Describe the morphology of the red blood cells.
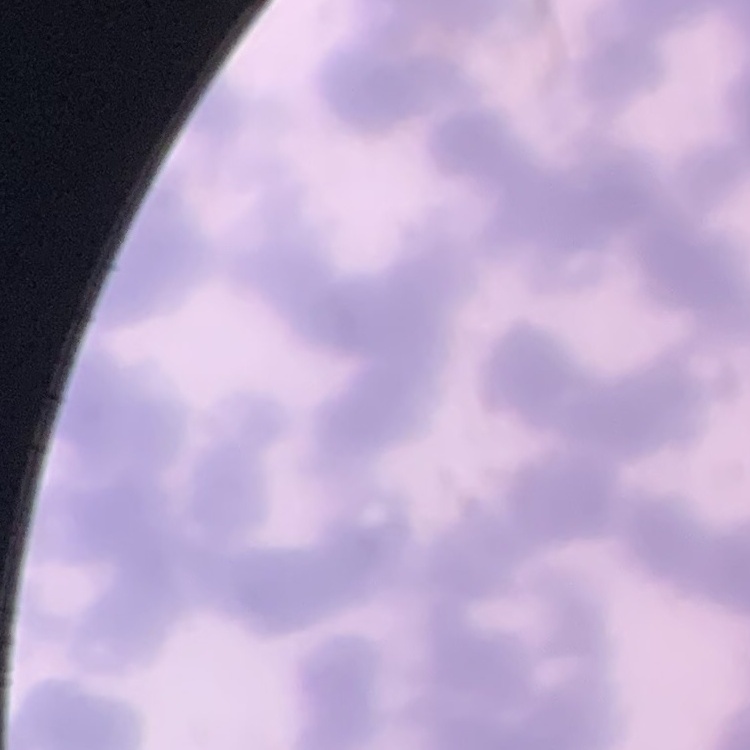

Rouleaux formation.

Summary:
  - Stain: Field's or Giemsa
  - Image type: square crop of a larger photomicrograph
  - Preparation: thin peripheral smear